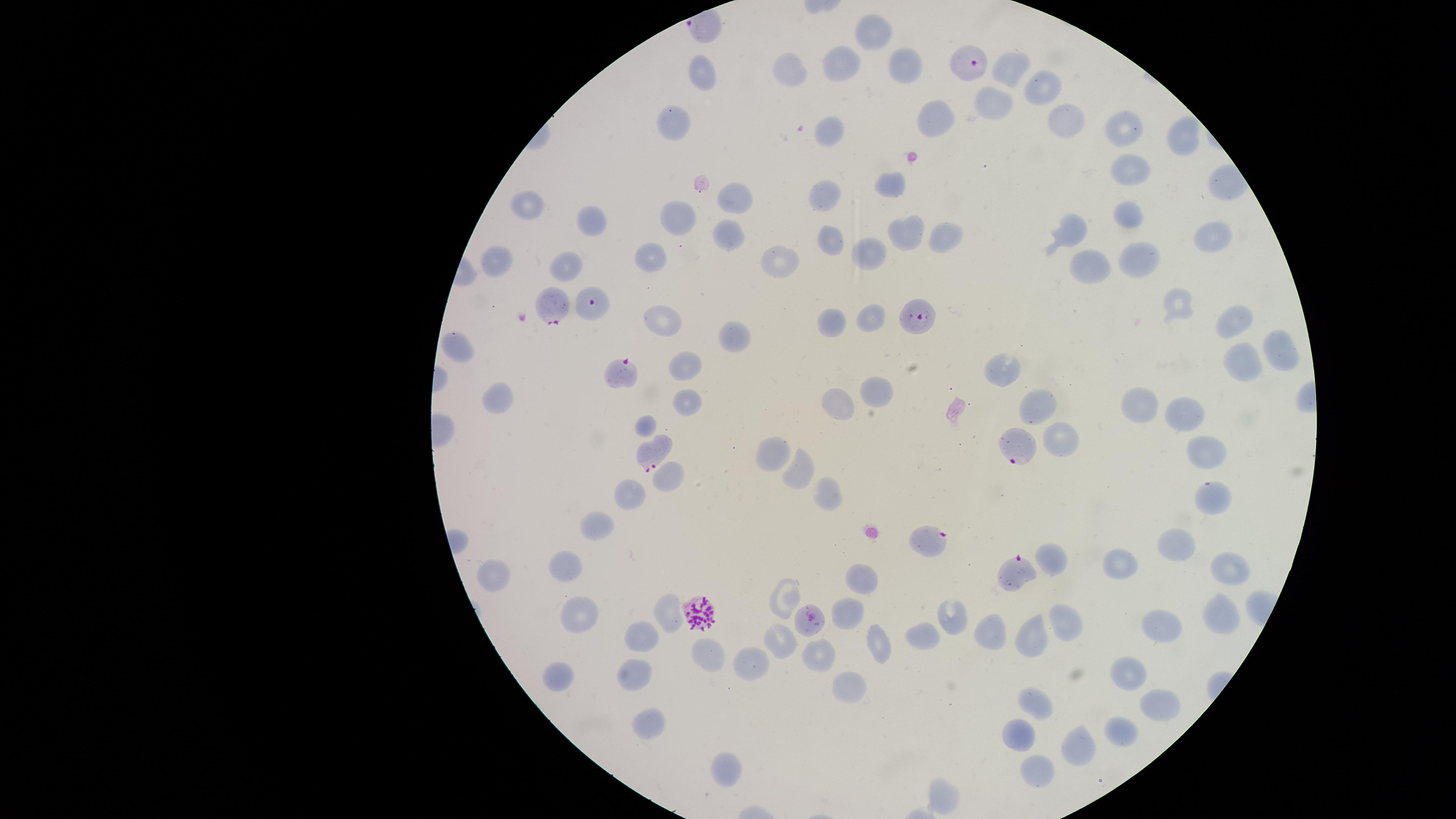
Approximate marker points as [x, y] in pixels.
Summary:
  - Uninfected red blood cells: [872, 28], [841, 62], [902, 65], [790, 68], [1010, 70], [704, 77], [1040, 87], [987, 111], [937, 114], [1062, 120], [674, 121], [1125, 125], [833, 132], [1184, 133], [1130, 169], [891, 183], [823, 192], [736, 197], [529, 204], [1124, 214], [676, 217], [593, 222], [1070, 224], [727, 230], [902, 231], [938, 234], [829, 238], [1208, 238], [867, 253], [651, 256], [1142, 258], [494, 261], [781, 261], [571, 265], [1086, 265], [1176, 304], [870, 316], [664, 318], [1232, 318], [835, 319], [737, 336], [1281, 345], [464, 350], [686, 359], [1240, 359], [1003, 366], [876, 389], [500, 397], [839, 402], [1144, 402], [686, 404], [1036, 410], [1185, 411], [650, 420], [1059, 435], [1206, 447], [773, 453], [798, 471], [667, 477], [825, 491], [628, 493], [1216, 497], [595, 527], [1177, 546], [1056, 556], [1123, 560], [1228, 565], [564, 566], [494, 567], [864, 576], [786, 598], [851, 607], [1220, 611], [949, 614], [581, 615], [664, 616], [1066, 621], [1161, 622], [993, 630], [642, 634], [920, 635], [1036, 638], [779, 640], [879, 645], [821, 654], [711, 655], [759, 658], [1131, 669], [640, 672], [557, 676], [844, 685], [1163, 700], [1036, 706], [651, 723], [1126, 723], [1020, 731], [1086, 741], [728, 770], [1040, 772], [947, 794]
  - Parasitized red blood cells: [962, 62], [550, 302], [594, 307], [913, 315], [626, 371], [1013, 446], [647, 450], [933, 543], [1010, 572], [701, 612], [809, 620]
  - Stain: Giemsa
  - Visible region: circular
  - Presence: malaria parasites identified
  - Preparation: thin blood smear
  - Field of view: single
  - Capture: smartphone photograph through the microscope eyepiece
  - Image size: 1456×819 pixels
  - Species: Plasmodium falciparum